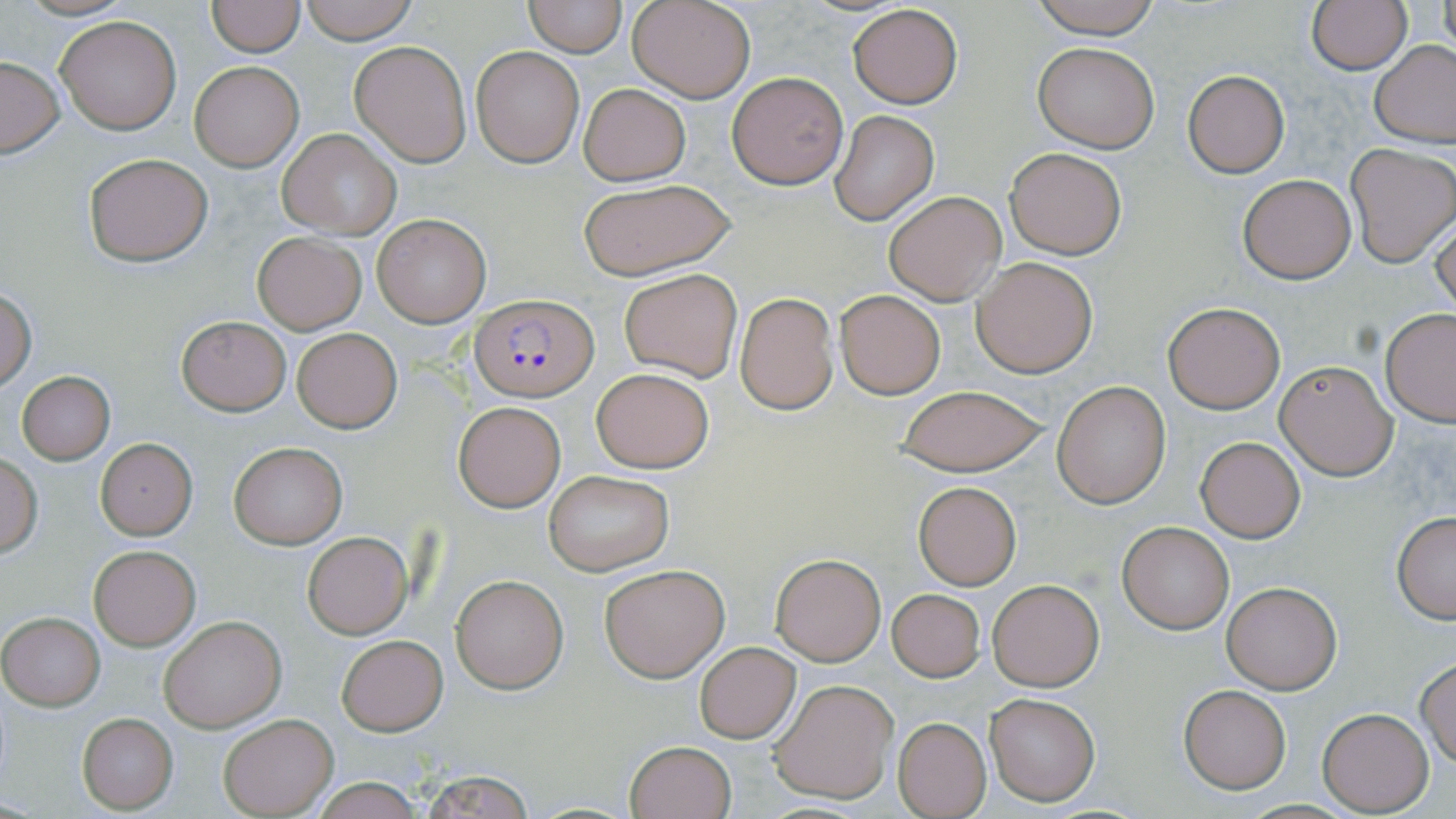
Plasmodium falciparum-infected red blood cell locations = approximate bounding boxes as (x1, y1, x2, y2) in pixels: (472, 295, 598, 403)
slide-level diagnosis = Plasmodium falciparum
preparation = thin blood film
field of view = one of a larger specimen
magnification = 1000x
modality = light microscopy
image size = 1456×819 pixels
stain = May-Grünwald-Giemsa
uninfected red blood cell locations = approximate bounding boxes as (x1, y1, x2, y2) in pixels: (14, 0, 138, 22), (297, 0, 418, 44), (628, 0, 755, 103), (1025, 0, 1166, 39), (1305, 0, 1412, 74), (208, 1, 303, 56), (522, 1, 628, 57), (1437, 2, 1455, 56), (847, 3, 964, 110), (55, 15, 182, 134), (1371, 39, 1456, 148), (349, 40, 471, 166), (1031, 41, 1160, 153), (471, 46, 584, 167), (0, 57, 65, 157), (190, 62, 303, 172), (1183, 70, 1290, 178), (727, 72, 849, 190), (579, 83, 691, 186), (830, 111, 938, 224), (276, 129, 401, 238), (1345, 143, 1456, 266), (1004, 145, 1127, 260), (83, 152, 212, 267), (1237, 173, 1356, 283), (577, 180, 735, 279), (884, 191, 1005, 305), (372, 211, 492, 328), (1431, 213, 1456, 321), (252, 232, 366, 335), (972, 256, 1097, 377), (618, 268, 742, 383), (0, 289, 36, 392), (835, 289, 945, 399), (735, 292, 838, 414), (1162, 302, 1285, 414), (1380, 309, 1456, 426), (175, 316, 291, 416), (293, 329, 402, 432), (1275, 360, 1397, 479), (591, 367, 714, 473), (16, 371, 115, 463), (1052, 381, 1171, 508), (892, 384, 1052, 475), (453, 401, 566, 513), (1195, 437, 1306, 542), (95, 438, 198, 539), (229, 442, 346, 548), (0, 452, 42, 556), (543, 470, 675, 576), (913, 481, 1021, 590), (1392, 510, 1456, 623), (1116, 521, 1233, 634), (301, 531, 414, 639), (88, 543, 201, 651), (770, 554, 884, 665), (599, 564, 729, 681), (450, 574, 568, 693), (1220, 579, 1343, 694), (988, 580, 1103, 692), (886, 588, 986, 681), (1, 613, 104, 710), (159, 614, 286, 732), (337, 635, 447, 735), (694, 641, 800, 744), (1415, 657, 1456, 767), (768, 680, 899, 804), (1179, 685, 1291, 792), (984, 691, 1101, 805), (1317, 706, 1434, 815), (77, 713, 178, 813), (218, 714, 338, 816), (892, 717, 991, 818), (624, 740, 736, 819), (415, 768, 538, 819), (305, 778, 429, 818)